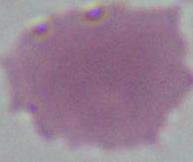

Summary:
  - Magnification: 1000x
  - Modality: photomicrograph
  - Identification: red blood cell